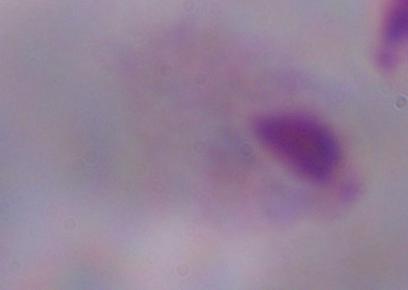

modality = photomicrograph
identification = trichomonad
magnification = 1000x